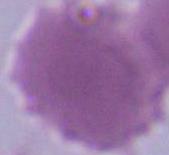

{
  "identification": "erythrocyte",
  "modality": "photomicrograph",
  "magnification": "1000x"
}